Locate every malaria parasite.
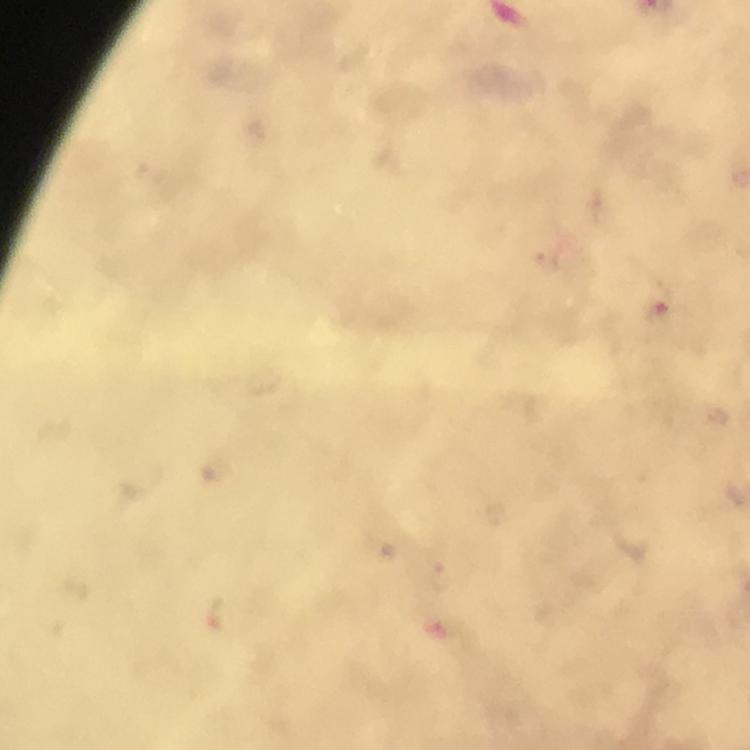

Approximate centers as [x, y] in pixels.
Malaria parasites: [659, 311], [217, 613].

Immersion oil was used. At 100x magnification. A crop from one field of view. Smartphone photograph taken through a microscope. Thick smear. From a malaria diagnostic workup. Giemsa stain. Image is 750×750 pixels.